Report the malaria status of this cell.
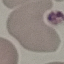

It is uninfected.

Thin blood smear. Photographed with a smartphone camera at the microscope eyepiece. Cell patch, automatically extracted from a larger field of view and resized to 64 × 64 pixels. Giemsa stain.